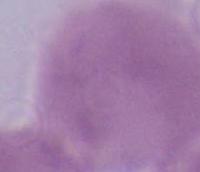

Summary:
  - Identification: red blood cell
  - Modality: photomicrograph
  - Magnification: 1000x